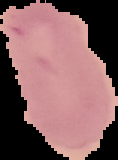 The area outside the segmented cell region is set to black. From a thin blood smear. Malaria status: uninfected. Image is 118×160 pixels.